State which parasite is depicted.
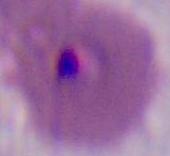

Plasmodium.

Summary:
  - Modality: micrograph
  - Magnification: 400x or 1000x